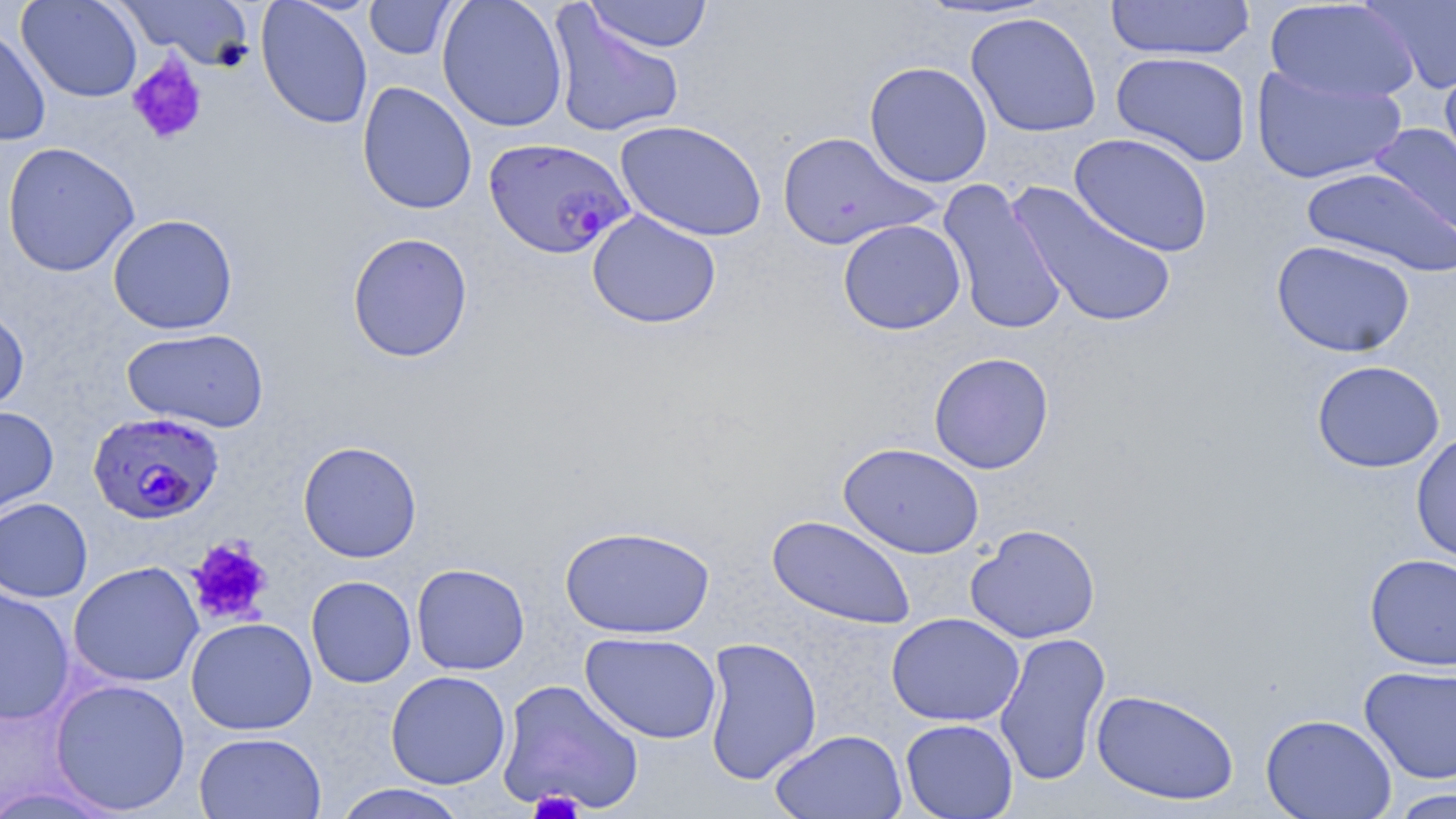 Approximate bounding boxes as [x1, y1, x2, y2] in pixels. Uninfected red blood cell locations: [16, 0, 143, 103], [115, 0, 255, 70], [437, 0, 568, 132], [583, 0, 713, 53], [1105, 0, 1256, 62], [1360, 0, 1456, 94], [256, 1, 373, 130], [365, 1, 458, 60], [1266, 1, 1421, 103], [547, 4, 686, 140], [965, 12, 1103, 138], [0, 24, 51, 147], [1110, 51, 1252, 167], [1439, 58, 1456, 185], [864, 61, 993, 187], [1251, 66, 1407, 185], [356, 82, 477, 215], [615, 119, 767, 241], [1368, 123, 1456, 243], [777, 130, 941, 251], [1068, 133, 1214, 257], [2, 141, 140, 277], [1302, 167, 1456, 277], [936, 178, 1069, 337], [1008, 181, 1178, 331], [586, 210, 721, 329], [107, 214, 238, 335], [838, 219, 966, 335], [347, 232, 473, 362], [1271, 239, 1415, 358], [0, 305, 30, 418], [122, 328, 270, 432], [929, 352, 1054, 474], [1311, 360, 1445, 473], [0, 406, 59, 523], [1411, 431, 1456, 566], [298, 440, 422, 563], [838, 442, 985, 559], [0, 497, 93, 602], [767, 514, 916, 631], [965, 523, 1101, 644], [559, 524, 715, 638], [1364, 553, 1456, 671], [68, 561, 204, 688], [411, 563, 530, 675], [306, 575, 417, 688], [0, 587, 75, 726], [886, 612, 1024, 727], [185, 617, 317, 735], [993, 630, 1111, 787], [580, 631, 722, 744], [701, 637, 822, 785], [1359, 664, 1456, 784], [386, 670, 511, 789], [50, 678, 191, 815], [496, 679, 644, 813], [1091, 688, 1239, 806], [1260, 713, 1396, 819], [900, 718, 1018, 818], [770, 729, 906, 818], [194, 731, 327, 819], [332, 784, 471, 819], [1383, 787, 1456, 818]. Plasmodium falciparum-infected red blood cell locations: [483, 137, 635, 259], [86, 410, 225, 525]. Platelet locations: [126, 55, 208, 146], [186, 537, 273, 627], [529, 788, 583, 819]. Slide-level diagnosis: Plasmodium falciparum. Captured at 1000x magnification. Thin blood film. Single field of view. May-Grünwald-Giemsa-stained preparation. Optical microscopy. Image is 1456×819 pixels.